Assess this cell for malaria.
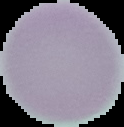
It is uninfected.

{
  "preparation": "thin blood film",
  "image_type": "segmented cell region on a black background",
  "image_size": "124×127 pixels"
}